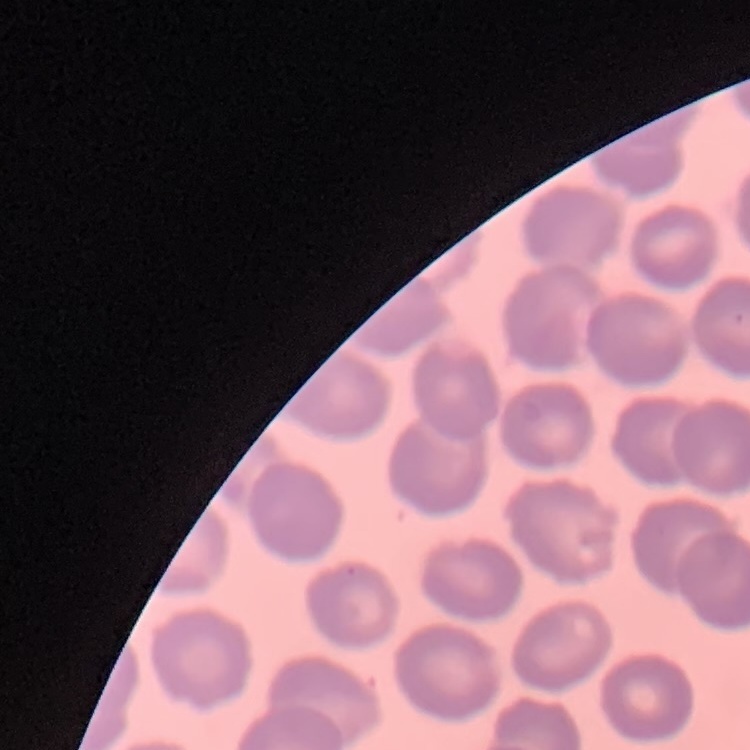
The red blood cells show no rouleaux formation. One tile cut from a larger photomicrograph. Thin blood smear. Stained with either Field's or Giemsa.